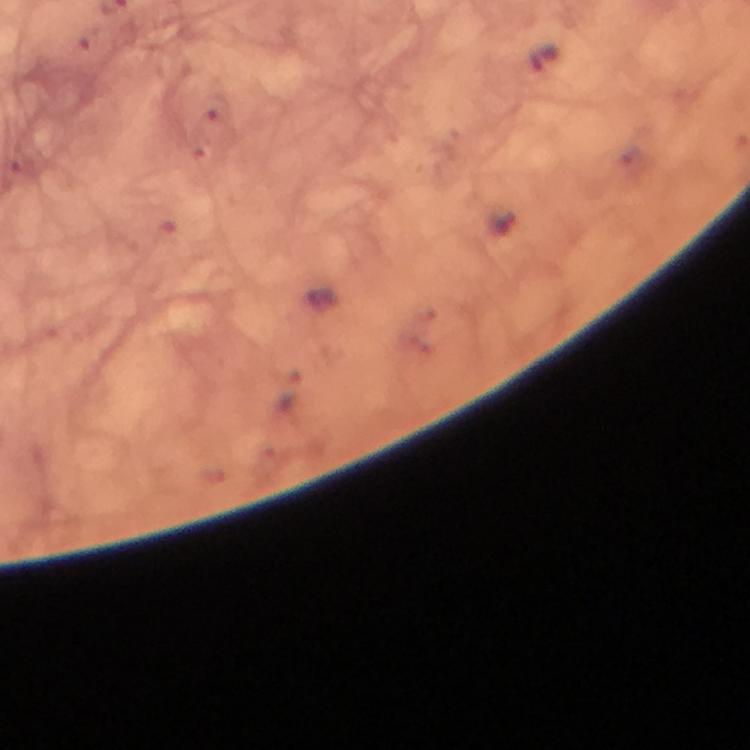 Approximate object centers, in pixels from the top-left corner. Malaria parasite locations: (x=545, y=57). Immersion oil applied. Smartphone photograph taken through a microscope. At 100x magnification. A crop from one field of view. Image is 750×750 pixels. Giemsa-stained preparation. From a diagnostic examination for malaria. Thick smear.